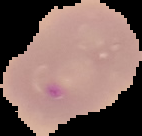

Malaria status: parasitized. Image is 142×136 pixels. From a thin blood film. Segmented cell region on a black background.